Identify the parasite.
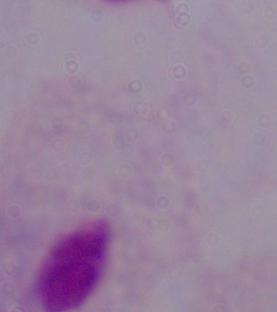
A trichomonad.

modality = micrograph
magnification = 1000x